Identify the cell.
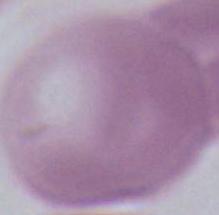
An erythrocyte.

Photomicrograph. 1000x magnification.